Comment on the morphology of the red blood cells.
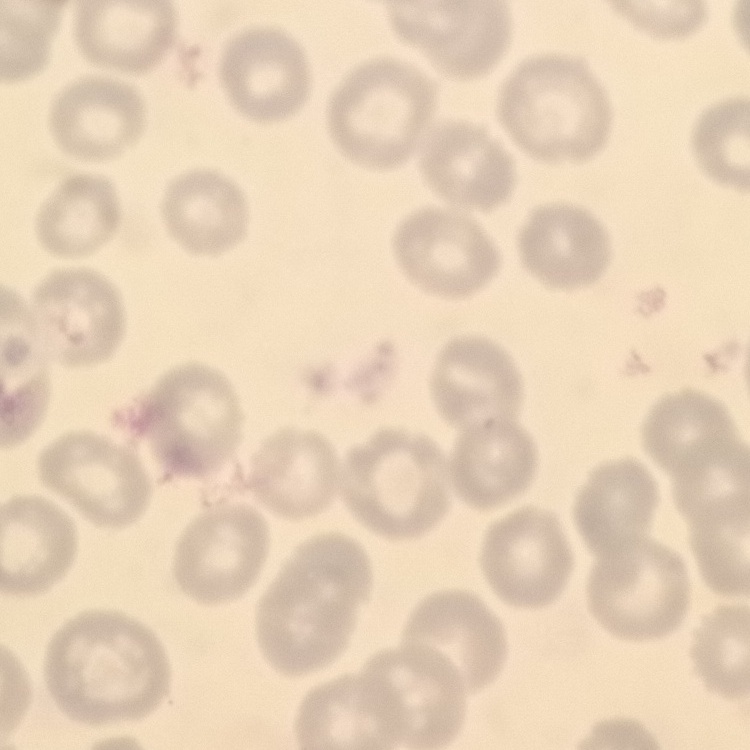

They show no rouleaux formation.

Square crop of a larger photomicrograph. Field's or Giemsa stain. Thin peripheral smear.